Assess for malaria.
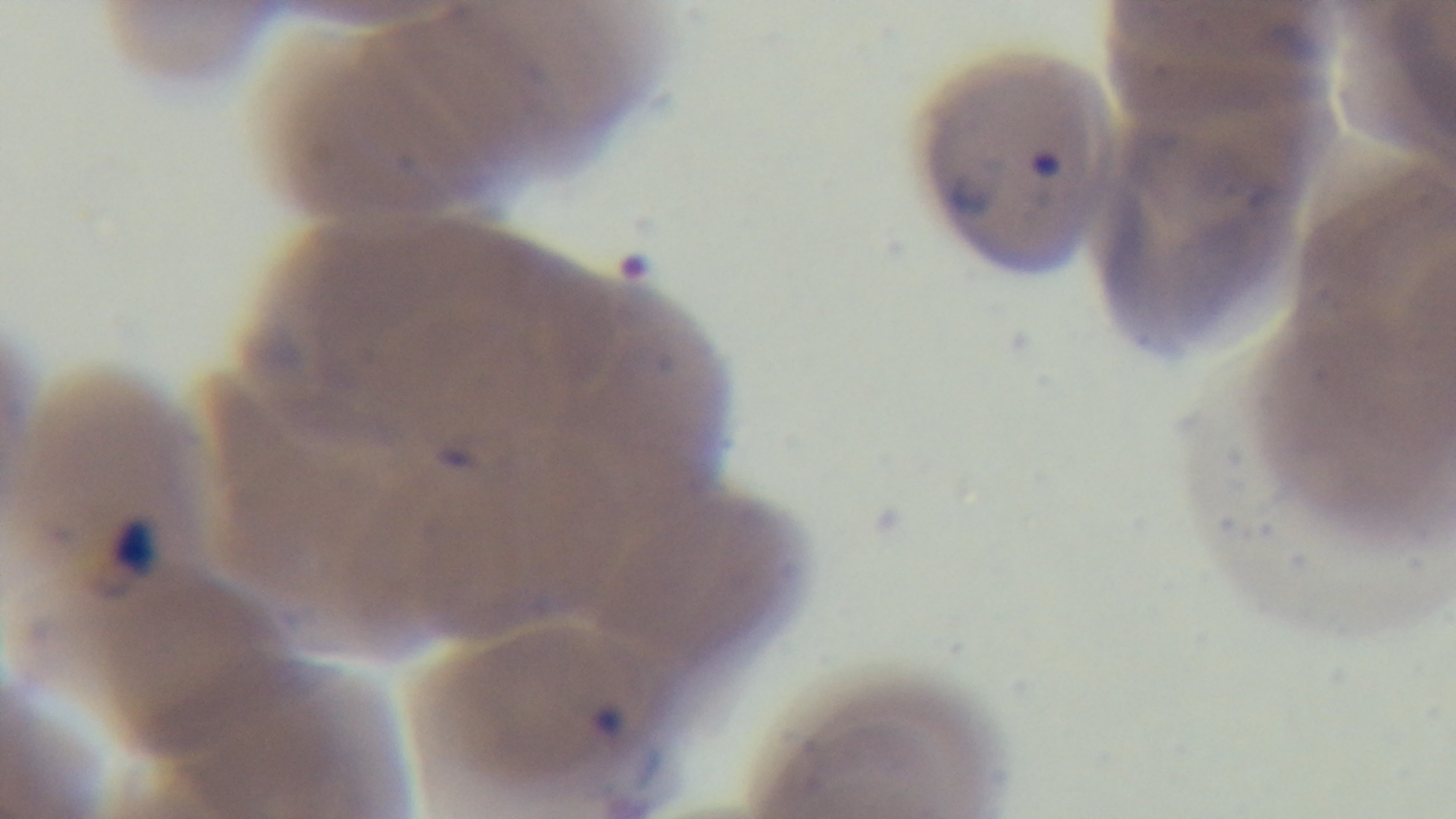

Infected.

{
  "objective": "100x oil immersion",
  "preparation": "thin blood film",
  "field_of_view": "single",
  "modality": "light microscopy",
  "capture": "mounted 4K digital camera",
  "stain": "Giemsa"
}